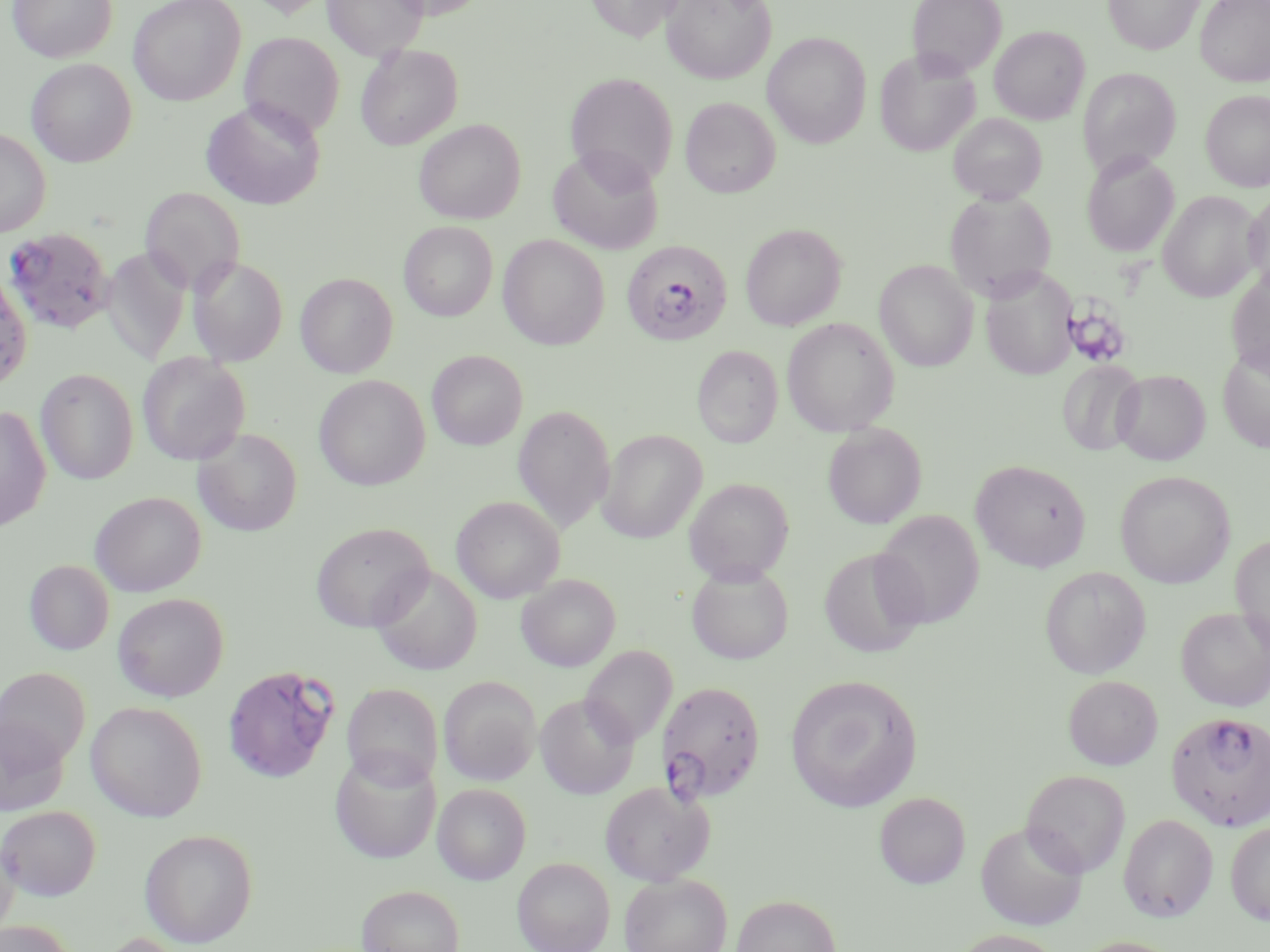

Summary:
  - Coordinate format: approximate bounding boxes as [x1, y1, x2, y2] in pixels
  - Platelet locations: [1062, 300, 1130, 368]
  - Uninfected red blood cell locations: [7, 0, 116, 62], [128, 0, 246, 105], [246, 0, 334, 18], [323, 0, 428, 60], [584, 0, 685, 41], [661, 0, 776, 84], [907, 0, 1006, 79], [1103, 0, 1203, 54], [1195, 0, 1270, 86], [989, 25, 1089, 124], [240, 32, 344, 139], [762, 32, 871, 148], [355, 44, 463, 150], [874, 49, 980, 157], [26, 58, 136, 167], [1078, 68, 1180, 176], [565, 72, 678, 187], [1200, 90, 1270, 192], [680, 97, 780, 198], [200, 99, 325, 211], [947, 112, 1047, 204], [414, 119, 525, 224], [0, 128, 51, 237], [547, 146, 665, 254], [1081, 150, 1179, 257], [140, 186, 244, 295], [1243, 189, 1270, 298], [945, 190, 1057, 301], [1158, 191, 1262, 302], [399, 221, 497, 321], [740, 223, 846, 331], [498, 234, 610, 350], [102, 247, 191, 364], [188, 256, 288, 366], [874, 259, 978, 371], [0, 265, 32, 391], [980, 266, 1078, 381], [1226, 268, 1270, 377], [295, 273, 397, 378], [781, 318, 900, 436], [1218, 343, 1270, 453], [693, 345, 782, 448], [427, 350, 528, 450], [137, 352, 250, 465], [1057, 359, 1145, 456], [35, 368, 139, 486], [1112, 369, 1210, 465], [313, 374, 431, 491], [0, 405, 51, 531], [512, 405, 616, 532], [823, 423, 927, 529], [194, 428, 302, 536], [597, 429, 707, 543], [971, 459, 1091, 572], [1115, 470, 1235, 588], [684, 477, 794, 584], [90, 491, 206, 596], [451, 496, 565, 603], [873, 510, 983, 629], [311, 521, 433, 632], [1231, 535, 1270, 654], [818, 548, 929, 658], [24, 559, 114, 655], [686, 562, 793, 664], [371, 565, 482, 675], [1040, 567, 1151, 678], [516, 574, 620, 671], [112, 592, 229, 701], [1177, 606, 1270, 712], [580, 645, 677, 746], [0, 667, 90, 769], [785, 674, 922, 812], [1063, 675, 1162, 770], [439, 676, 541, 785], [342, 683, 443, 789], [535, 694, 639, 798], [86, 700, 206, 822], [0, 715, 70, 816], [329, 749, 441, 864], [1021, 770, 1131, 877], [599, 780, 714, 886], [433, 783, 531, 884], [874, 792, 970, 889], [0, 805, 101, 899], [1119, 814, 1219, 922], [1225, 820, 1270, 925], [976, 822, 1087, 930], [139, 828, 258, 948], [0, 831, 20, 940], [513, 857, 614, 952], [619, 873, 732, 952], [356, 884, 464, 952], [732, 894, 842, 952], [0, 921, 77, 952], [950, 929, 1065, 952], [1069, 935, 1187, 952]
  - Plasmodium falciparum-infected red blood cell locations: [2, 227, 114, 335], [621, 240, 733, 346], [222, 664, 339, 784], [657, 679, 766, 803], [1166, 711, 1270, 832]
  - Slide-level diagnosis: Plasmodium falciparum
  - Modality: optical microscopy
  - Stain: May-Grünwald-Giemsa
  - Preparation: thin blood film
  - Magnification: 1000x
  - Image size: 1270×952 pixels
  - Field of view: one of a larger specimen